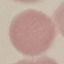
malaria status = uninfected
preparation = thin smear
image type = automatically extracted cell patch, resized to 64 × 64 pixels
stain = Giemsa
capture = smartphone through the microscope eyepiece